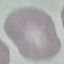
Summary:
  - Malaria status: uninfected
  - Stain: Giemsa
  - Capture: smartphone through the microscope eyepiece
  - Preparation: thin blood film
  - Image type: cell patch, automatically extracted from a larger field of view and resized to 64 × 64 pixels